Report the malaria status of this cell.
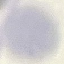
Uninfected.

Giemsa stain. Automatically extracted cell patch, resized to 64 × 64 pixels. Photographed with a smartphone camera at the microscope eyepiece. Thin blood film.